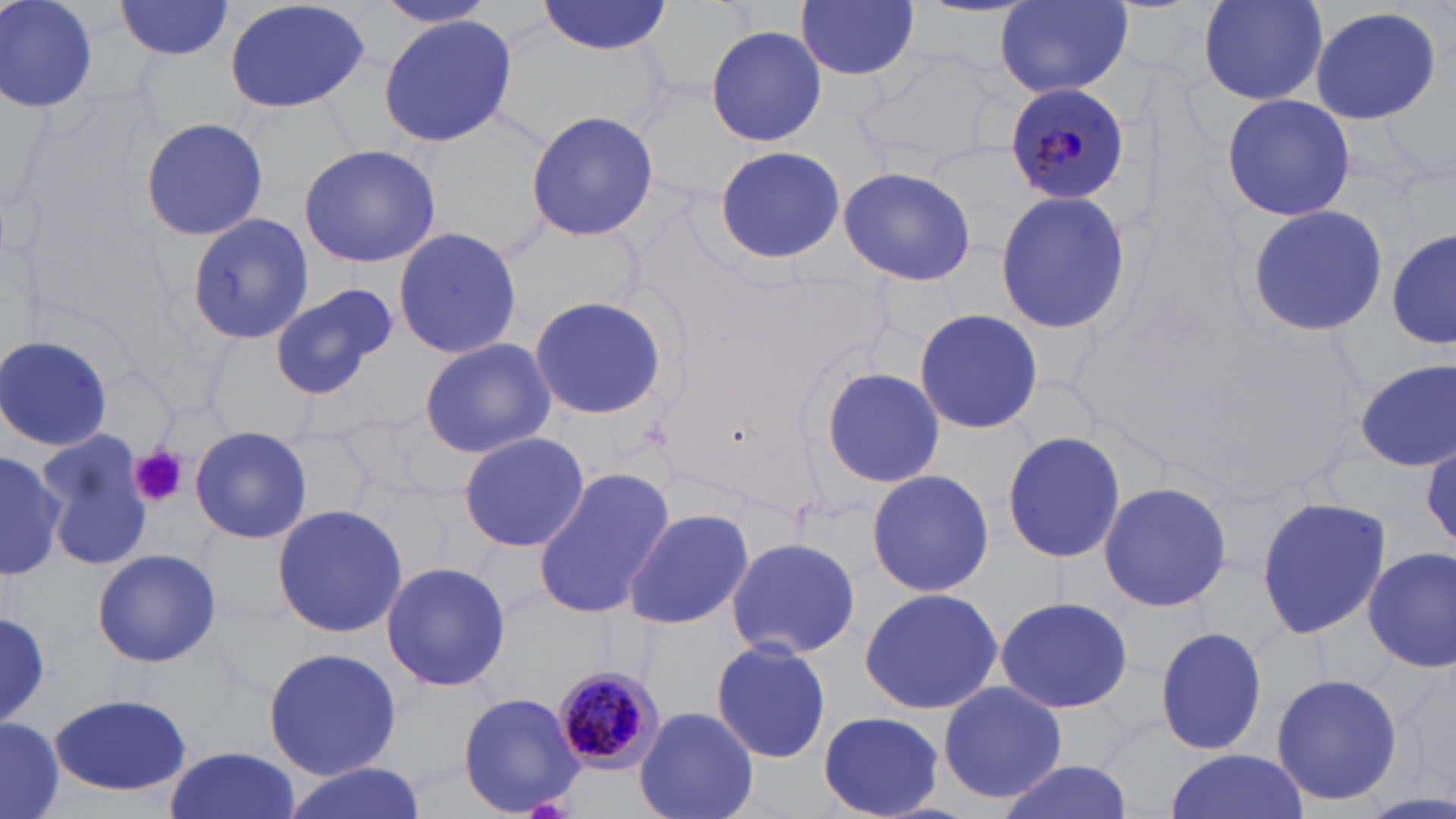 Approximate bounding boxes as (x1,y1)-(x2,y2) corner pairs in pixels. Platelet locations: (132,445)-(189,508). Uninfected red blood cell locations: (1,0)-(98,116), (115,0)-(234,60), (222,0)-(373,115), (374,0)-(498,28), (995,0)-(1133,98), (1196,0)-(1331,106), (537,1)-(671,55), (797,1)-(919,81), (1309,4)-(1444,126), (379,17)-(517,146), (703,24)-(827,147), (855,44)-(1000,171), (1220,93)-(1356,221), (525,111)-(659,242), (140,117)-(267,242), (300,143)-(441,268), (713,144)-(844,265), (835,166)-(978,285), (993,190)-(1132,333), (1246,204)-(1388,338), (185,214)-(314,344), (393,226)-(522,359), (1388,229)-(1454,352), (269,280)-(397,399), (526,295)-(669,421), (913,309)-(1043,434), (0,335)-(115,453), (419,338)-(554,457), (1354,360)-(1454,472), (819,367)-(947,489), (188,425)-(315,544), (37,429)-(153,574), (1001,429)-(1127,564), (457,431)-(590,554), (0,450)-(65,573), (532,467)-(674,621), (866,469)-(993,597), (1097,481)-(1234,614), (1254,493)-(1391,642), (269,503)-(409,638), (621,506)-(755,633), (1291,518)-(1456,662), (724,534)-(862,661), (1363,545)-(1455,673), (90,548)-(222,668), (380,561)-(512,693), (859,586)-(1002,716), (993,594)-(1134,714), (0,612)-(53,726), (1153,626)-(1269,755), (710,638)-(832,764), (262,647)-(403,779), (1272,670)-(1402,808), (937,681)-(1068,806), (457,691)-(587,817), (49,695)-(191,794), (635,705)-(759,819), (815,709)-(947,818), (1,720)-(65,819), (162,746)-(299,819), (1160,749)-(1311,819), (993,760)-(1134,819), (278,763)-(427,819). Plasmodium malariae-infected red blood cell locations: (1005,80)-(1130,206), (547,663)-(668,775). Slide-level diagnosis: Plasmodium malariae. Single field of view. Image is 1456×819 pixels. 1000x magnification. May-Grünwald-Giemsa stain. Optical microscopy. Thin blood smear.